Give the position of every malaria parasite.
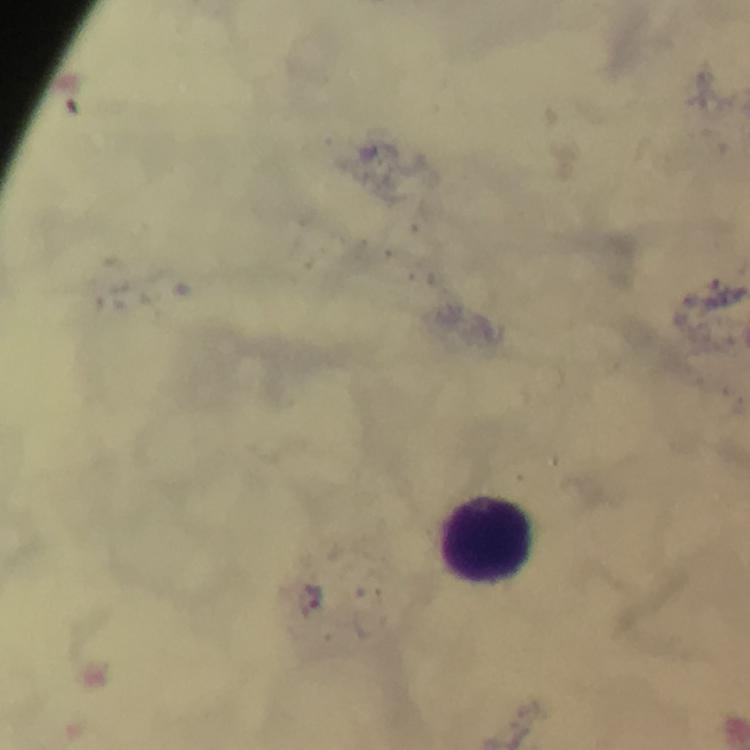

Approximate centers as (x, y) in pixels.
Malaria parasites: (315, 597).

capture = smartphone photograph through a microscope
image size = 750×750 pixels
magnification = 100x
stain = Giemsa
context = from a diagnostic examination for malaria
immersion oil = used
preparation = thick blood smear
leukocyte locations = approximate centers as (x, y) in pixels: (485, 542)
cropped from = one field of view